Describe the morphology of the red blood cells.
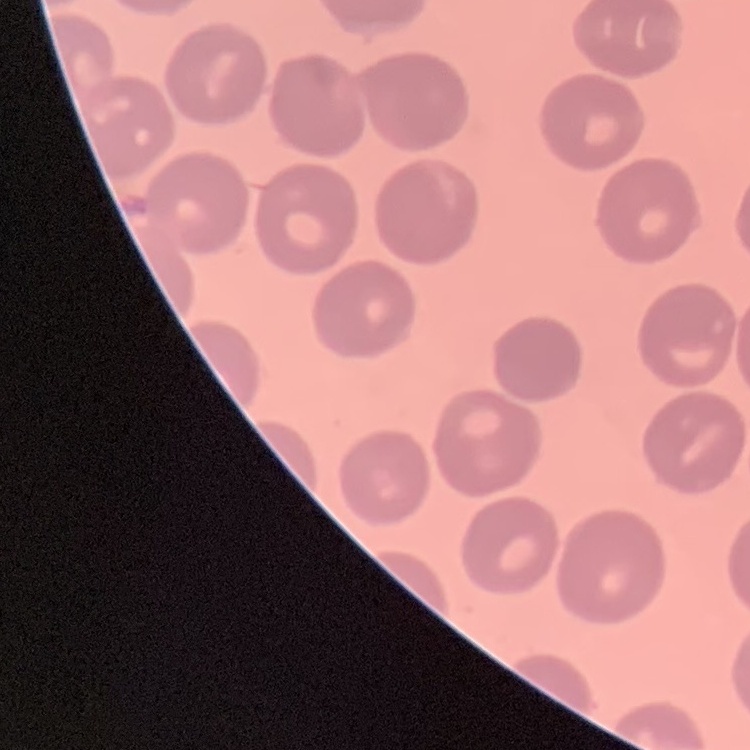

No rouleaux formation.

Field's or Giemsa stain. Thin blood smear. One tile cut from a larger photomicrograph.